Classify this cell by malaria status.
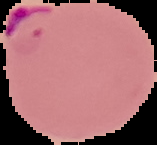
It is parasitized.

From a thin blood smear. Cell region segmented out of the field of view; the surrounding area is masked to black. Image is 157×145 pixels.